State the blood parasite species.
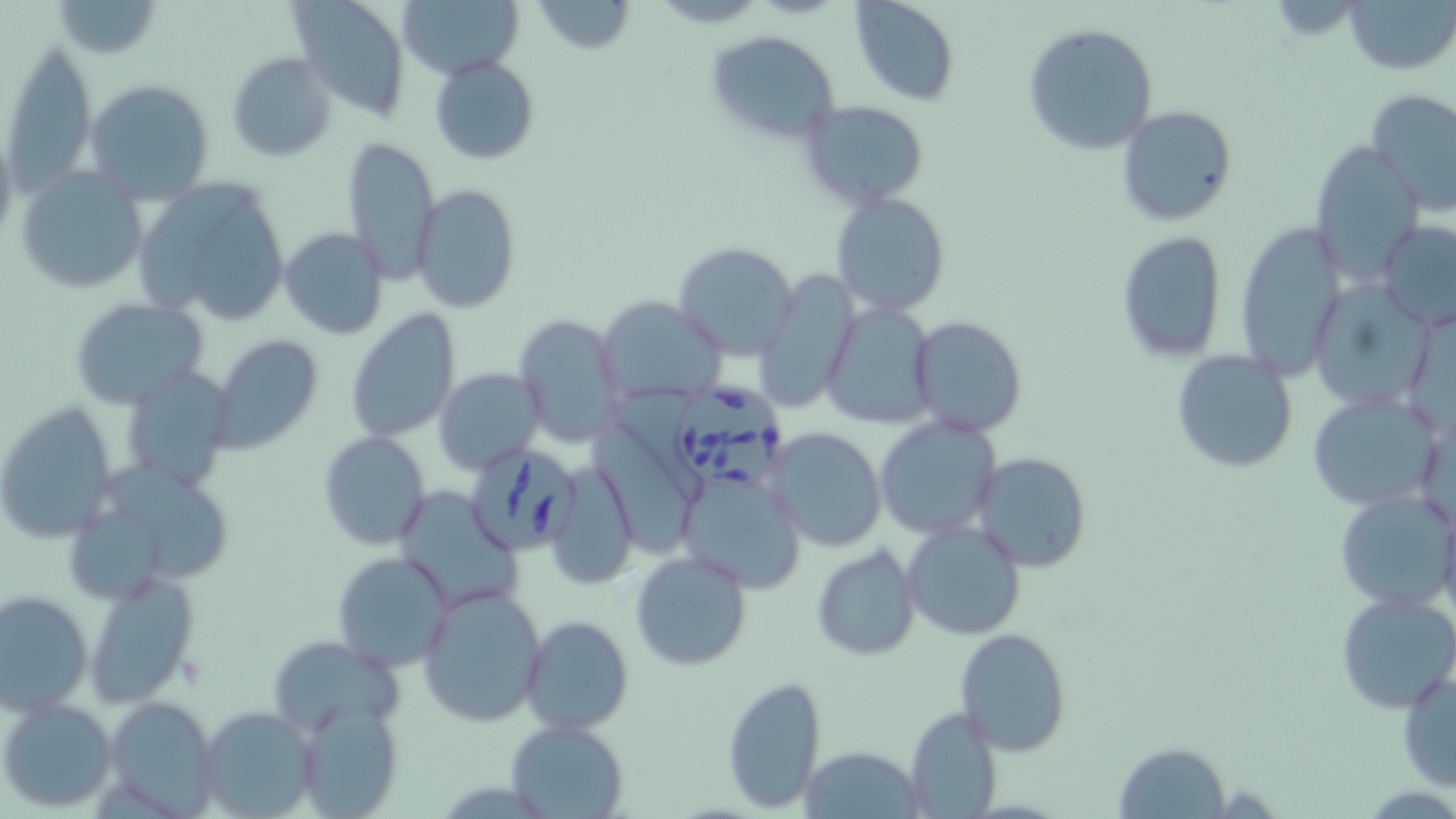

Babesia divergens.

{
  "modality": "optical microscopy",
  "field_of_view": "one of a larger specimen",
  "magnification": "1000x",
  "preparation": "thin blood film",
  "stain": "May-Grünwald-Giemsa",
  "image_size": "1456×819 pixels",
  "babesia_divergens_infected_red_blood_cell_locations": "approximate bounding boxes as (x1, y1, x2, y2) in pixels: (677, 384, 786, 491), (474, 444, 583, 558)",
  "uninfected_red_blood_cell_locations": "approximate bounding boxes as (x1, y1, x2, y2) in pixels: (287, 0, 414, 118), (394, 0, 520, 77), (850, 0, 960, 106), (1346, 0, 1455, 73), (531, 1, 634, 54), (1023, 23, 1158, 155), (703, 29, 841, 144), (3, 37, 98, 189), (226, 52, 337, 161), (430, 55, 539, 164), (84, 79, 215, 205), (1367, 90, 1456, 214), (797, 101, 930, 209), (1116, 105, 1237, 226), (341, 137, 442, 285), (1309, 139, 1423, 281), (15, 165, 147, 295), (134, 178, 289, 327), (411, 184, 520, 315), (830, 191, 950, 317), (1233, 217, 1347, 378), (1377, 219, 1456, 331), (279, 227, 387, 341), (1116, 232, 1227, 362), (673, 241, 800, 360), (756, 270, 857, 415), (1317, 274, 1433, 407), (596, 295, 729, 406), (68, 297, 208, 409), (820, 302, 938, 428), (344, 309, 461, 443), (513, 314, 626, 449), (911, 316, 1026, 437), (208, 333, 325, 454), (1170, 348, 1298, 473), (117, 365, 232, 492), (433, 368, 544, 476), (1305, 391, 1440, 511), (0, 401, 119, 542), (873, 416, 999, 539), (592, 420, 692, 547), (767, 427, 886, 552), (318, 432, 429, 550), (971, 452, 1091, 571), (546, 465, 636, 590), (673, 466, 806, 595), (388, 485, 526, 610), (1335, 487, 1453, 609), (902, 520, 1027, 641), (812, 545, 920, 660), (629, 550, 752, 672), (331, 551, 456, 674), (83, 570, 199, 706), (417, 582, 547, 726), (0, 589, 94, 715), (1335, 590, 1456, 715), (520, 615, 633, 736), (954, 628, 1070, 754), (268, 634, 403, 737), (1397, 665, 1455, 793), (721, 675, 826, 813), (105, 694, 221, 813), (0, 697, 117, 812), (288, 702, 405, 818), (196, 704, 318, 815), (901, 706, 1003, 818), (504, 719, 627, 818), (1113, 741, 1231, 817), (800, 744, 924, 817)"
}